Assess the morphology of the erythrocytes.
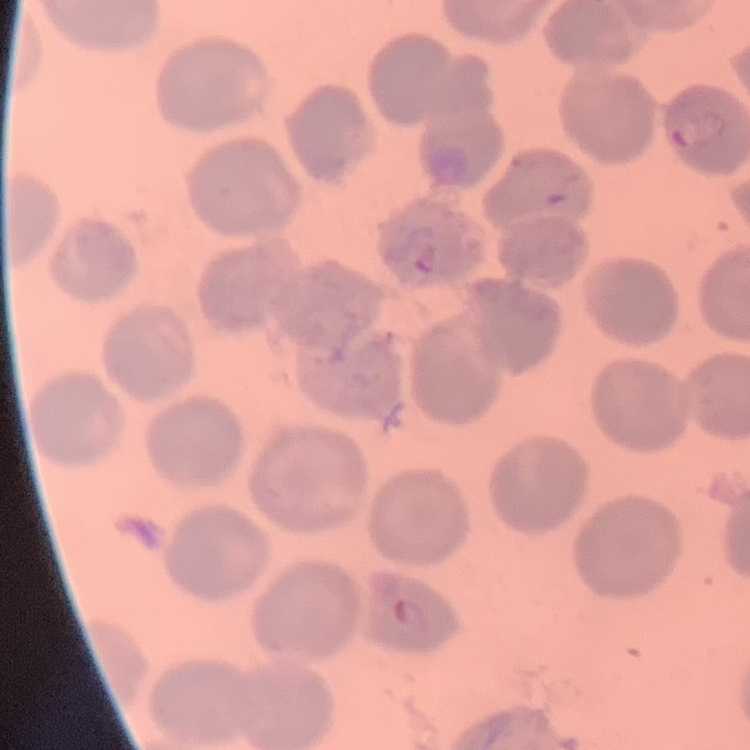

They show no rouleaux formation.

Summary:
  - Image type: one tile cut from a larger photomicrograph
  - Stain: Field's or Giemsa
  - Preparation: thin peripheral smear